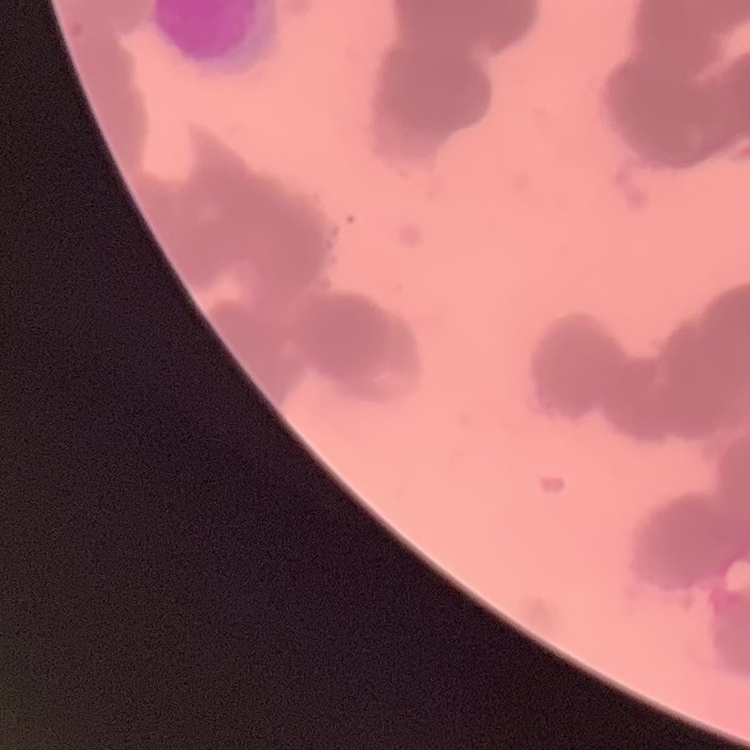 The erythrocytes show rouleaux formation. Stained with either Field's or Giemsa. One tile cut from a larger photomicrograph. Thin blood film.